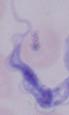

modality: micrograph
magnification: 1000x
identification: trypanosome